Report the malaria status of this cell.
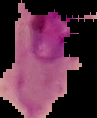

It is parasitized.

Summary:
  - Image type: segmented cell region on a black background
  - Image size: 97×118 pixels
  - Preparation: thin blood film